Assess this cell for malaria.
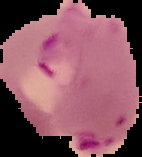

Parasitized.

From a thin blood film. Image is 142×157 pixels. Segmented cell region on a black background.